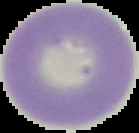

{
  "image_type": "cell region segmented out of the field of view; surrounding area masked to black",
  "result": "negative for Plasmodium parasites",
  "image_size": "139×133 pixels",
  "preparation": "thin blood film"
}